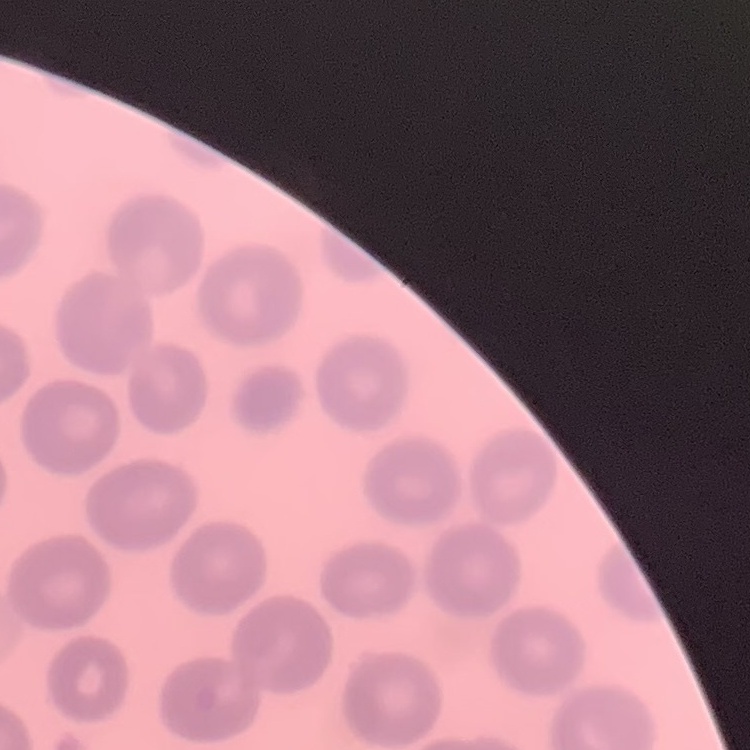 The red blood cells exhibit no rouleaux formation. Thin peripheral smear. Field's or Giemsa stain. Square crop of a larger photomicrograph.